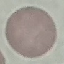 Result: no malaria parasites seen. Photographed with a smartphone camera at the microscope eyepiece. Giemsa stain. Automatically extracted cell patch, resized to 64 × 64 pixels. Thin blood smear.